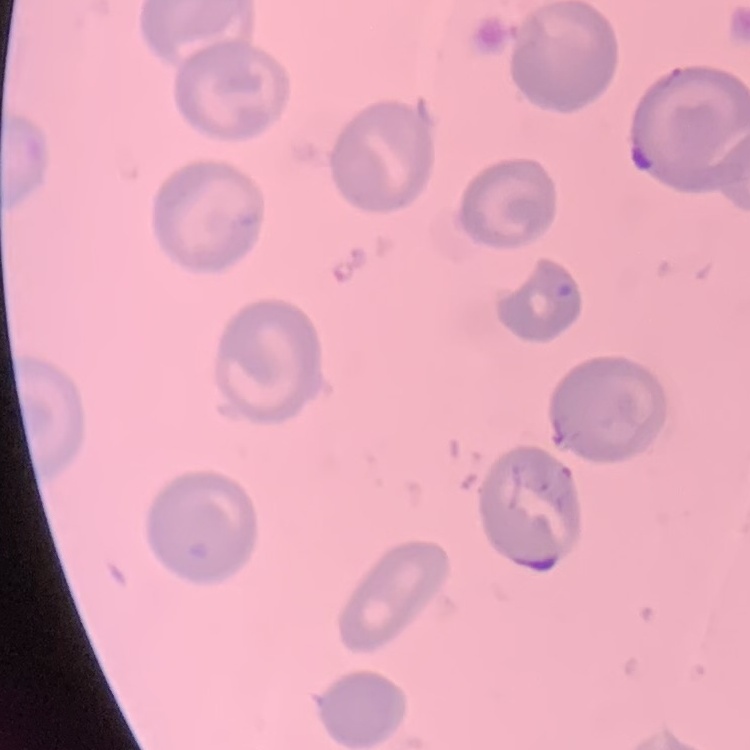
The red blood cells show no rouleaux formation. Thin peripheral smear. Square crop of a larger photomicrograph. Stained with either Field's or Giemsa.